Classify this cell by malaria status.
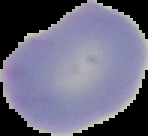

Uninfected.

From a thin blood smear. Image is 148×136 pixels. The area outside the segmented cell region is set to black.